Report the malaria status of this cell.
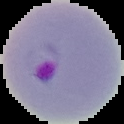
It is parasitized.

image type = cell region segmented out of the field of view; surrounding area masked to black
preparation = thin blood smear
image size = 124×124 pixels